Assess this cell for malaria.
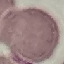
It is uninfected.

capture = smartphone through the microscope eyepiece
stain = Giemsa
image type = cell patch, automatically extracted from a larger field of view and resized to 64 × 64 pixels
preparation = thin blood film